Classify this cell by malaria status.
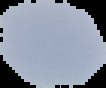
Uninfected.

Segmented cell region on a black background. Image is 106×88 pixels. From a thin blood film.